Assess the morphology of the erythrocytes.
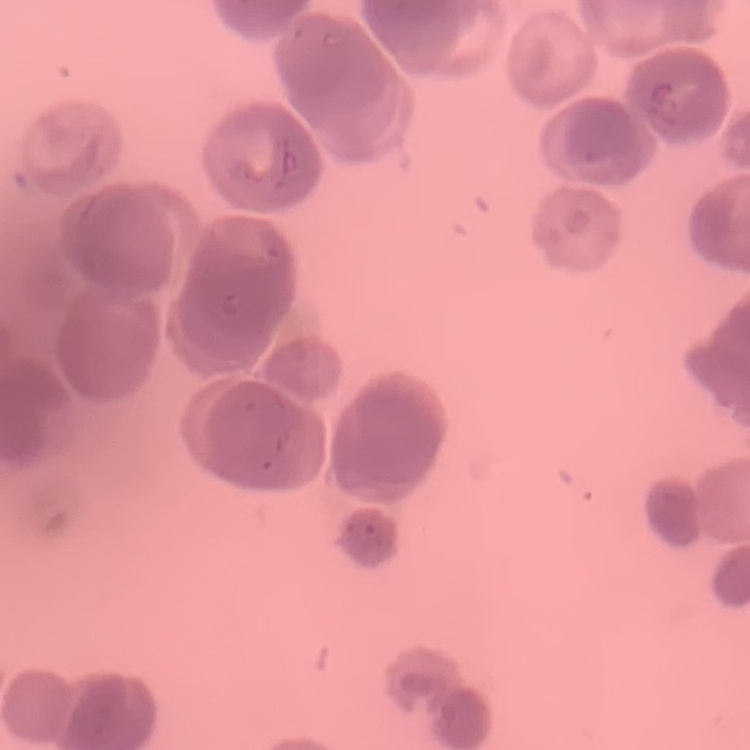
Rouleaux formation.

preparation: thin blood smear
image_type: square crop of a larger photomicrograph
stain: Field's or Giemsa